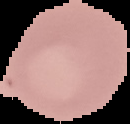

image size = 130×124 pixels
preparation = thin blood film
malaria status = uninfected
image type = segmented cell region with the area outside set to black